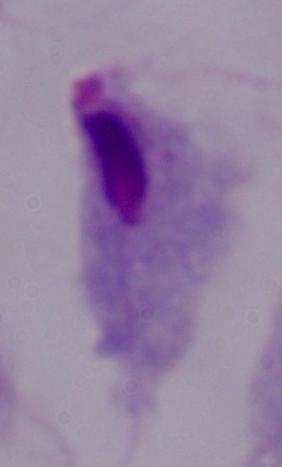
identification = trichomonad
modality = photomicrograph
magnification = 1000x